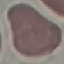

Summary:
  - Result: no malaria parasites detected
  - Stain: Giemsa
  - Preparation: thin smear
  - Image type: automatically extracted cell patch, resized to 64 × 64 pixels
  - Capture: smartphone camera at the microscope eyepiece